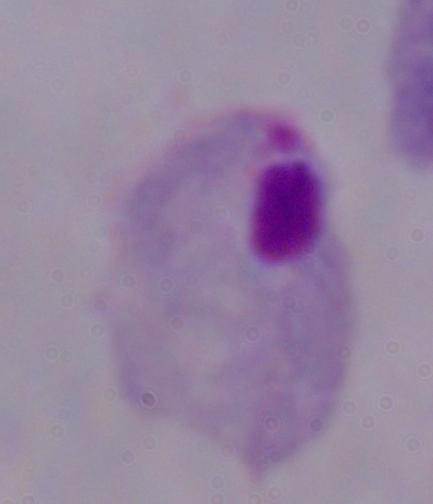
identification = trichomonad
magnification = 1000x
modality = micrograph